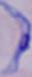

modality = micrograph
magnification = 1000x
identification = trypanosome